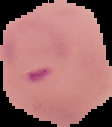
From a thin blood film. Segmented cell region on a black background. Image is 112×127 pixels. Result: malaria parasites identified.